State which cell type is depicted.
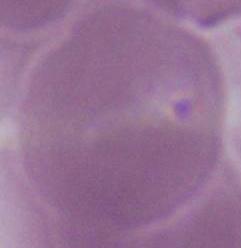
This is an erythrocyte.

Summary:
  - Magnification: 1000x
  - Modality: photomicrograph